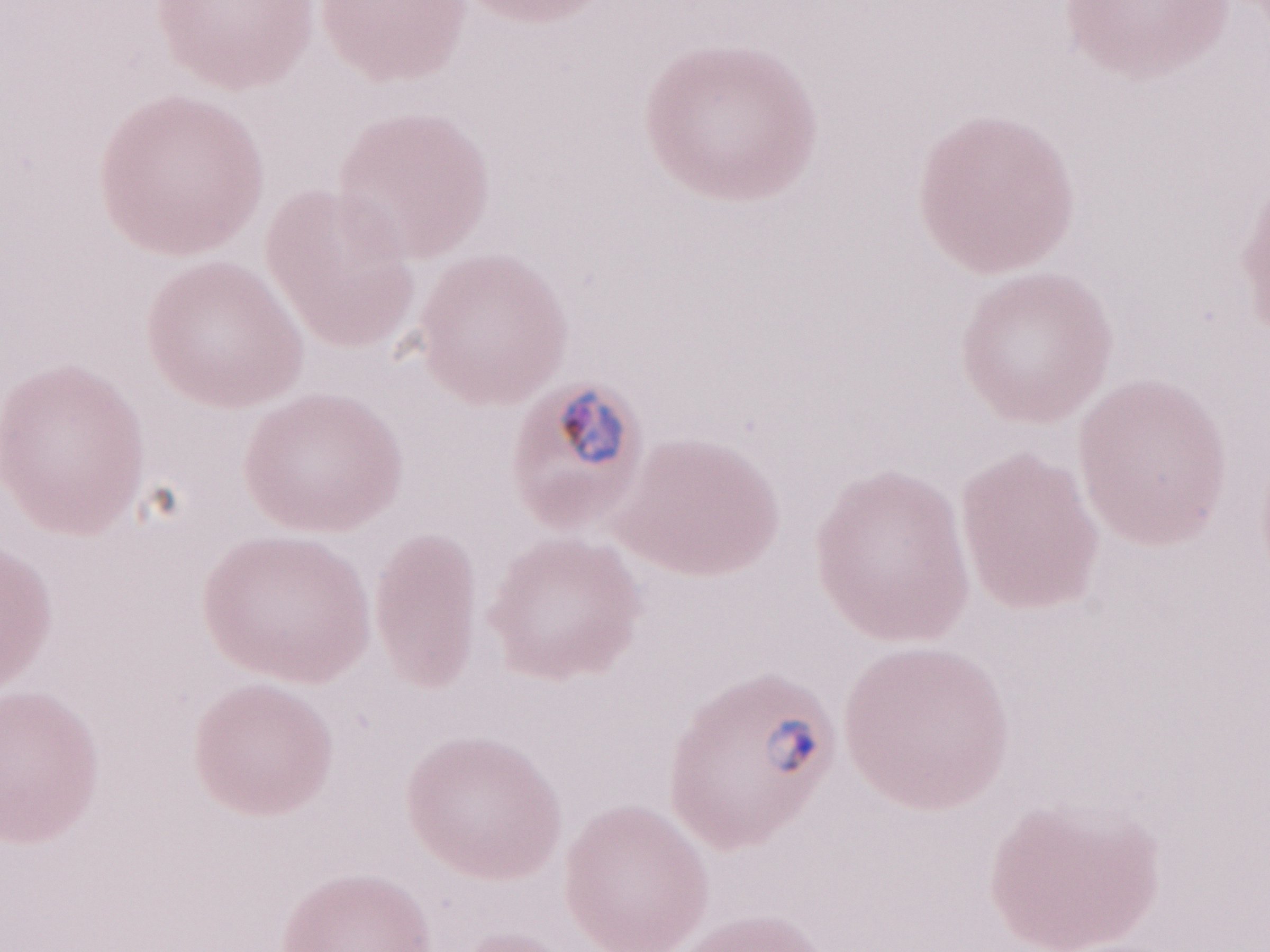

Olympus BX43 microscope, Olympus DP73 camera. 1,000x magnification. Malaria diagnosis (patient-level): positive. Thin blood smear. May-Grünwald-Giemsa (MGG) stain. Image is 1270×952 pixels. One field of this slide.